Give the position of every Plasmodium parasite, noting whether each is a trophozoite, schizont, or gametocyte.
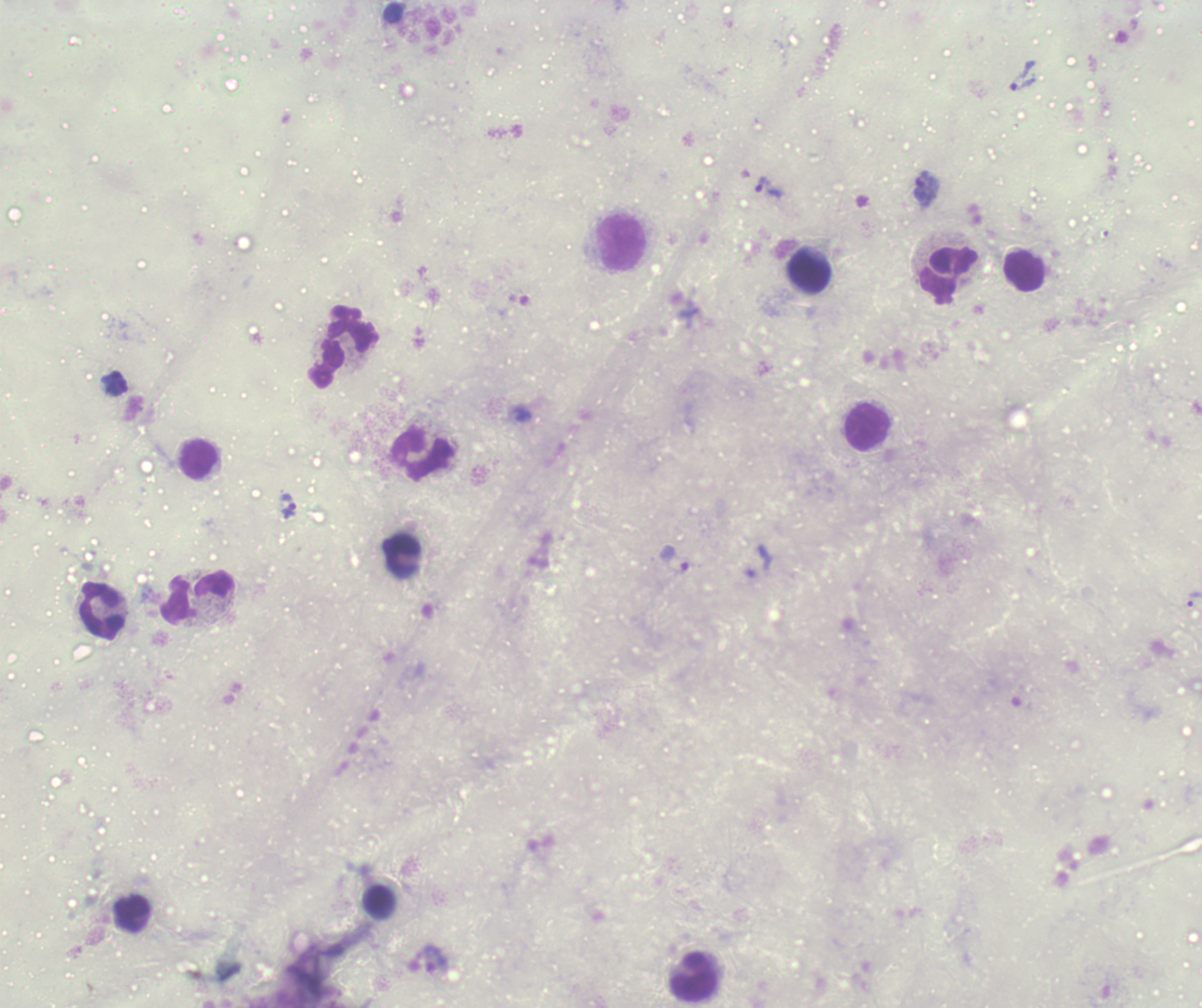

Approximate centers as (x, y) in pixels.
Trophozoites: (1024, 76), (769, 188), (927, 190), (115, 388), (291, 512), (676, 560), (1194, 599).
No schizont or gametocyte forms observed.

coordinate format = approximate centers as (x, y) in pixels
leukocyte locations = (623, 243), (1025, 271), (810, 272), (950, 272), (345, 345), (868, 426), (423, 454), (199, 460), (199, 598), (103, 610), (379, 901), (133, 913), (695, 977)
coloration quality = bad
background quality = unsatisfactory
field of view = single
image size = 1202×1008 pixels
preparation = thick smear of blood
magnification = 100x
stain = Romanowsky
context = previously used in an actual diagnosis